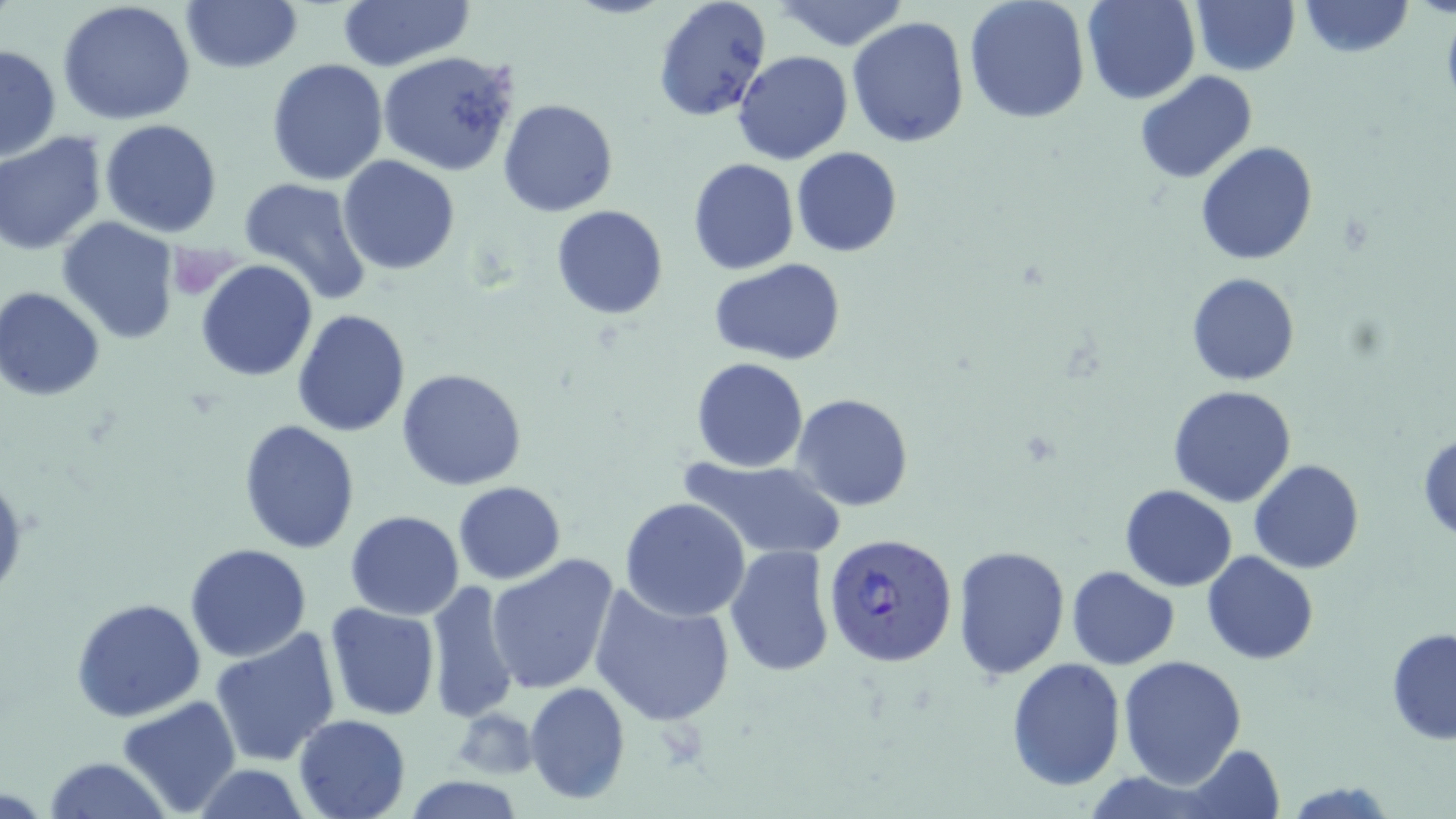
slide_level_diagnosis: Plasmodium falciparum
field_of_view: one of a larger specimen
image_size: 1456×819 pixels
modality: light microscopy
preparation: thin blood smear
stain: May-Grünwald-Giemsa
uninfected_red_blood_cell_locations: 'approximate bounding boxes as [x1, y1, x2, y2] in pixels: [58, 0, 196, 126], [335, 0, 475, 72], [652, 0, 775, 122], [777, 0, 910, 51], [1081, 0, 1200, 104], [1299, 0, 1413, 57], [181, 1, 302, 74], [965, 1, 1091, 123], [1191, 1, 1299, 75], [846, 15, 971, 147], [1, 43, 62, 163], [733, 49, 851, 165], [379, 51, 521, 176], [266, 58, 389, 186], [1134, 70, 1257, 185], [498, 99, 619, 218], [100, 119, 221, 238], [0, 131, 106, 254], [1195, 140, 1320, 265], [791, 146, 904, 258], [338, 156, 459, 275], [687, 158, 799, 274], [238, 177, 374, 303], [552, 204, 668, 319], [57, 221, 180, 343], [195, 259, 318, 381], [712, 259, 844, 365], [1187, 272, 1301, 385], [1, 288, 105, 400], [292, 308, 411, 437], [690, 357, 809, 472], [397, 368, 527, 491], [1167, 385, 1297, 507], [791, 392, 913, 512], [239, 420, 361, 555], [1417, 432, 1456, 544], [678, 458, 850, 562], [1248, 459, 1364, 573], [452, 481, 566, 584], [1119, 484, 1239, 591], [620, 497, 751, 622], [344, 510, 465, 620], [184, 544, 312, 662], [724, 545, 836, 677], [952, 545, 1072, 681], [1202, 552, 1318, 665], [486, 553, 621, 694], [1066, 565, 1180, 670], [425, 580, 523, 723], [590, 582, 735, 725], [71, 596, 205, 722], [323, 603, 440, 721], [210, 628, 342, 768], [1386, 629, 1456, 744], [1118, 654, 1247, 787], [1006, 659, 1126, 790], [524, 682, 630, 804], [114, 697, 243, 818], [453, 709, 541, 778], [294, 712, 411, 819], [1180, 744, 1285, 818], [43, 757, 173, 819], [189, 764, 312, 819], [401, 778, 528, 817], [1283, 780, 1399, 818]'
magnification: 1000x
plasmodium_falciparum_infected_red_blood_cell_locations: 'approximate bounding boxes as [x1, y1, x2, y2] in pixels: [822, 531, 959, 667]'